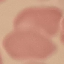
malaria status = uninfected
preparation = thin smear
capture = smartphone through the microscope eyepiece
image type = automatically extracted cell patch, resized to 64 × 64 pixels
stain = Giemsa